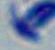
{
  "magnification": "1000x",
  "identification": "Toxoplasma gondii",
  "modality": "photomicrograph"
}